Assess the morphology of the erythrocytes.
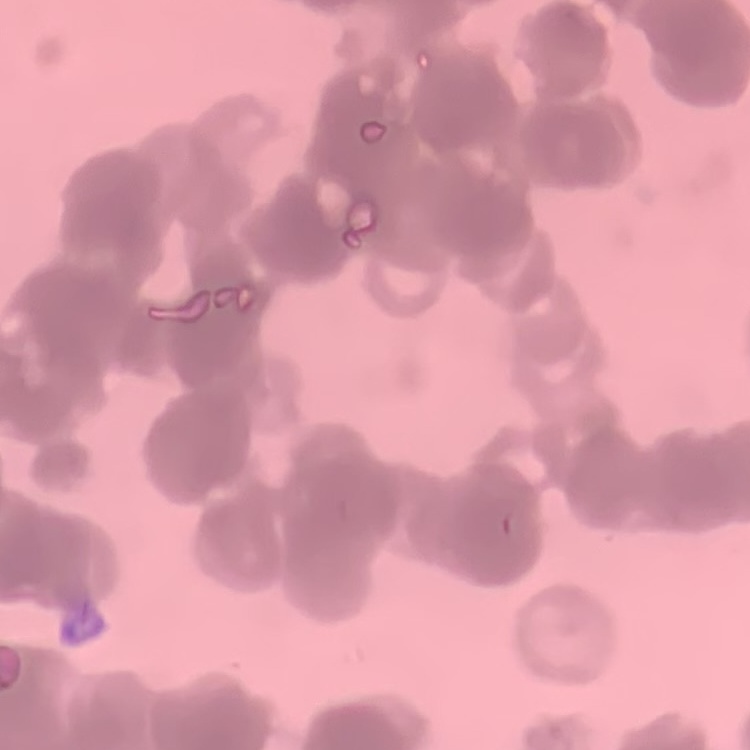

They show rouleaux formation.

stain = Field's or Giemsa
preparation = thin peripheral smear
image type = one tile cut from a larger photomicrograph